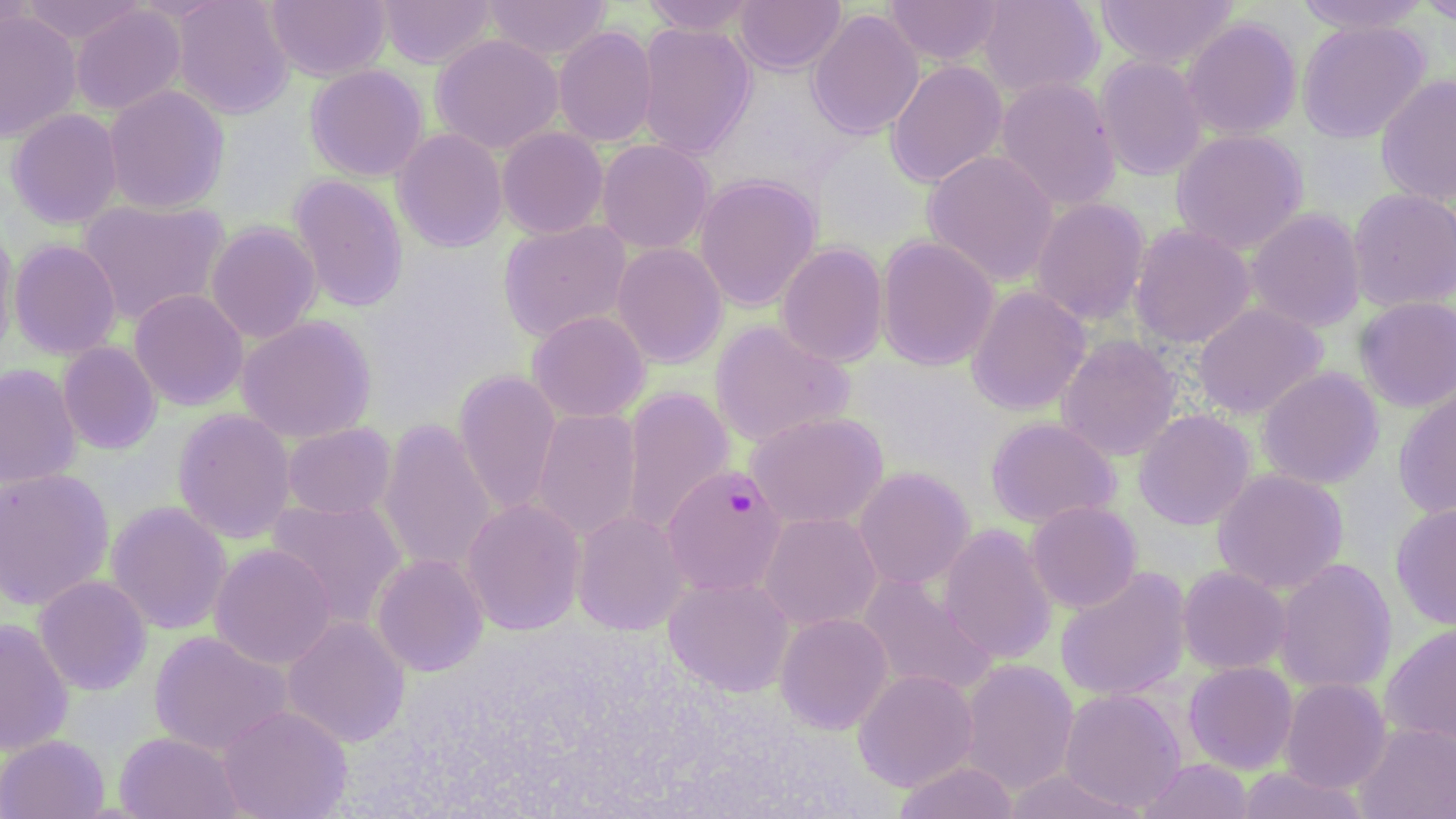
Approximate bounding boxes as (x1,y1)-(x2,y2) corner pairs in pixels. Plasmodium falciparum-infected red blood cell locations: (662,464)-(787,596). Uninfected red blood cell locations: (20,0)-(145,45), (171,0)-(294,119), (266,0)-(391,82), (375,0)-(497,69), (481,0)-(612,62), (734,0)-(846,74), (884,0)-(1004,66), (977,0)-(1104,99), (1095,0)-(1238,69), (1295,0)-(1431,35), (1417,0)-(1456,26), (641,1)-(759,36), (70,4)-(187,116), (807,8)-(924,140), (0,9)-(82,142), (1181,17)-(1302,140), (1297,19)-(1430,143), (636,22)-(757,159), (553,26)-(658,147), (430,33)-(564,154), (1094,55)-(1207,181), (885,60)-(1008,188), (305,64)-(429,182), (1376,74)-(1456,206), (994,76)-(1121,212), (103,84)-(230,215), (7,108)-(123,229), (496,126)-(609,239), (392,128)-(508,252), (1171,129)-(1308,254), (596,139)-(714,254), (922,150)-(1060,287), (289,173)-(409,312), (694,174)-(821,312), (1347,187)-(1456,312), (1030,197)-(1150,326), (77,198)-(230,326), (1245,208)-(1366,332), (0,218)-(19,363), (498,219)-(632,342), (205,221)-(322,343), (1129,223)-(1256,349), (876,234)-(999,371), (9,239)-(122,360), (611,242)-(728,368), (775,242)-(889,368), (966,285)-(1092,415), (129,288)-(248,411), (1354,296)-(1456,412), (1192,303)-(1327,419), (527,310)-(650,422), (236,315)-(377,444), (710,319)-(854,448), (1055,334)-(1182,461), (57,341)-(162,454), (0,363)-(82,489), (1257,367)-(1384,490), (453,369)-(561,515), (1393,385)-(1456,522), (620,386)-(736,536), (531,407)-(641,542), (173,408)-(296,544), (1133,409)-(1256,530), (746,411)-(888,530), (377,417)-(497,576), (985,417)-(1120,528), (282,422)-(397,520), (854,466)-(974,590), (0,468)-(115,610), (1212,468)-(1348,594), (265,496)-(408,628), (461,498)-(586,636), (1026,500)-(1142,613), (105,501)-(232,635), (1390,502)-(1456,630), (572,510)-(690,635), (759,512)-(882,631), (938,523)-(1057,665), (210,543)-(336,670), (371,554)-(488,676), (1274,557)-(1397,695), (1177,565)-(1292,675), (1054,566)-(1192,702), (857,573)-(998,699), (33,575)-(152,695), (664,575)-(794,697), (775,612)-(893,734), (282,616)-(410,747), (0,618)-(73,756), (1380,623)-(1456,751), (149,630)-(293,756), (959,659)-(1079,795), (1184,661)-(1298,774), (852,669)-(978,791), (1279,678)-(1392,794), (1058,688)-(1187,813), (217,704)-(353,819), (1355,723)-(1456,818), (115,731)-(243,819), (0,734)-(110,819), (1138,758)-(1255,819), (893,760)-(1019,819), (1235,766)-(1370,819), (1002,768)-(1145,819). Slide-level diagnosis: Plasmodium falciparum. Single field of view. May-Grünwald-Giemsa-stained preparation. Light microscopy. Image is 1456×819 pixels. 1000x magnification. Thin blood smear.